Describe the morphology of the erythrocytes.
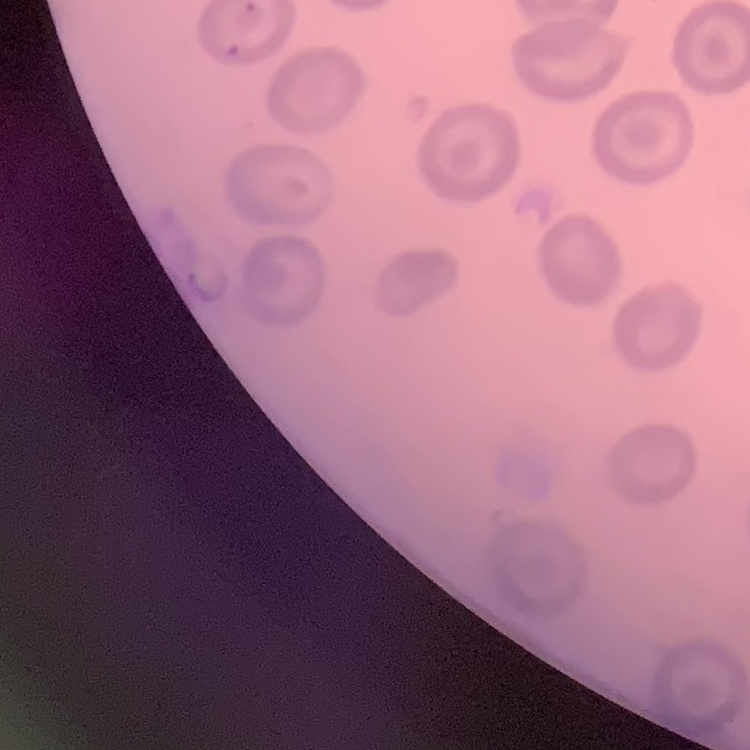

They show no rouleaux formation.

image type = one tile cut from a larger photomicrograph
preparation = thin blood film
stain = Field's or Giemsa